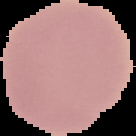

preparation: thin blood film
image_type: segmented cell region on a black background
image_size: 136×136 pixels
malaria_status: uninfected